State which parasite is depicted.
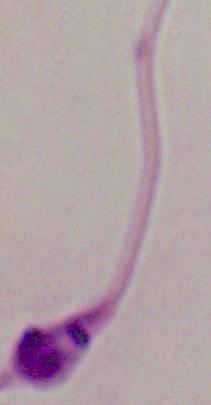

This is Leishmania.

1000x magnification. Photomicrograph.